Assess the morphology of the erythrocytes.
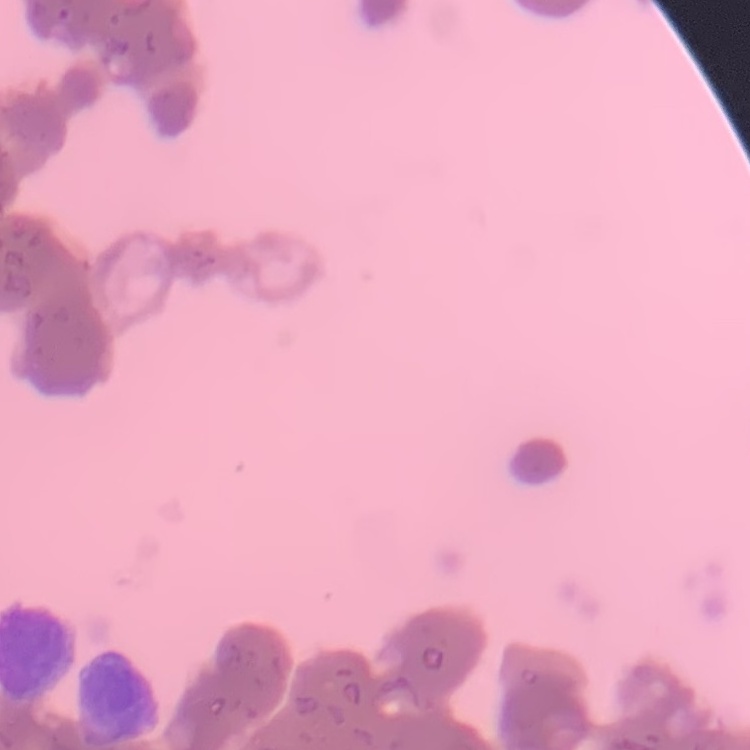
Rouleaux formation.

{
  "image_type": "one tile cut from a larger photomicrograph",
  "stain": "Field's or Giemsa",
  "preparation": "thin peripheral smear"
}